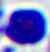 A white blood cell is seen. Captured at 400x magnification. Micrograph.